Classify this cell by malaria status.
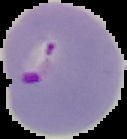
It is parasitized.

Summary:
  - Image size: 127×139 pixels
  - Preparation: thin blood smear
  - Image type: segmented cell region on a black background